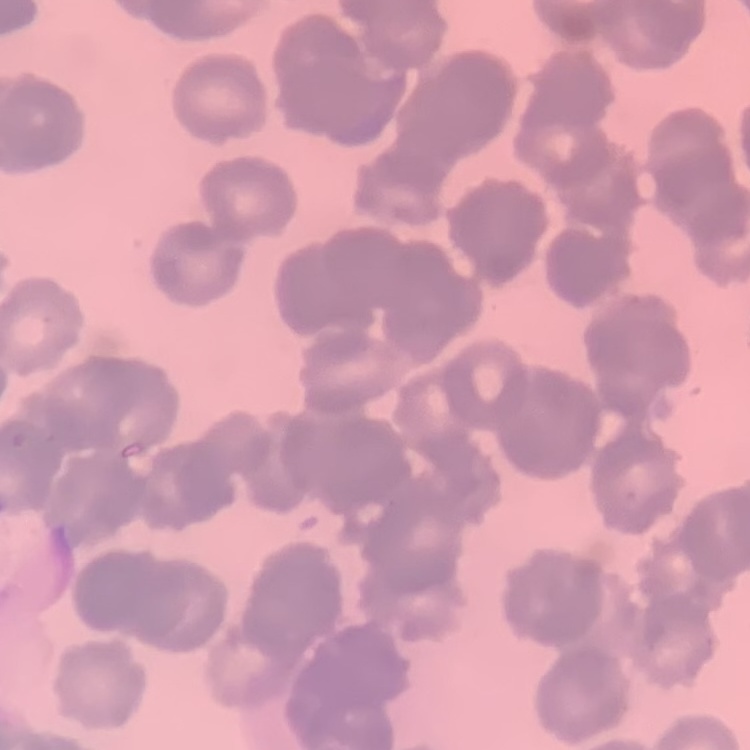

Summary:
  - Red blood cell morphology: rouleaux formation
  - Preparation: thin peripheral smear
  - Image type: square crop of a larger photomicrograph
  - Stain: Field's or Giemsa